Point out each Plasmodium parasite and each leukocyte.
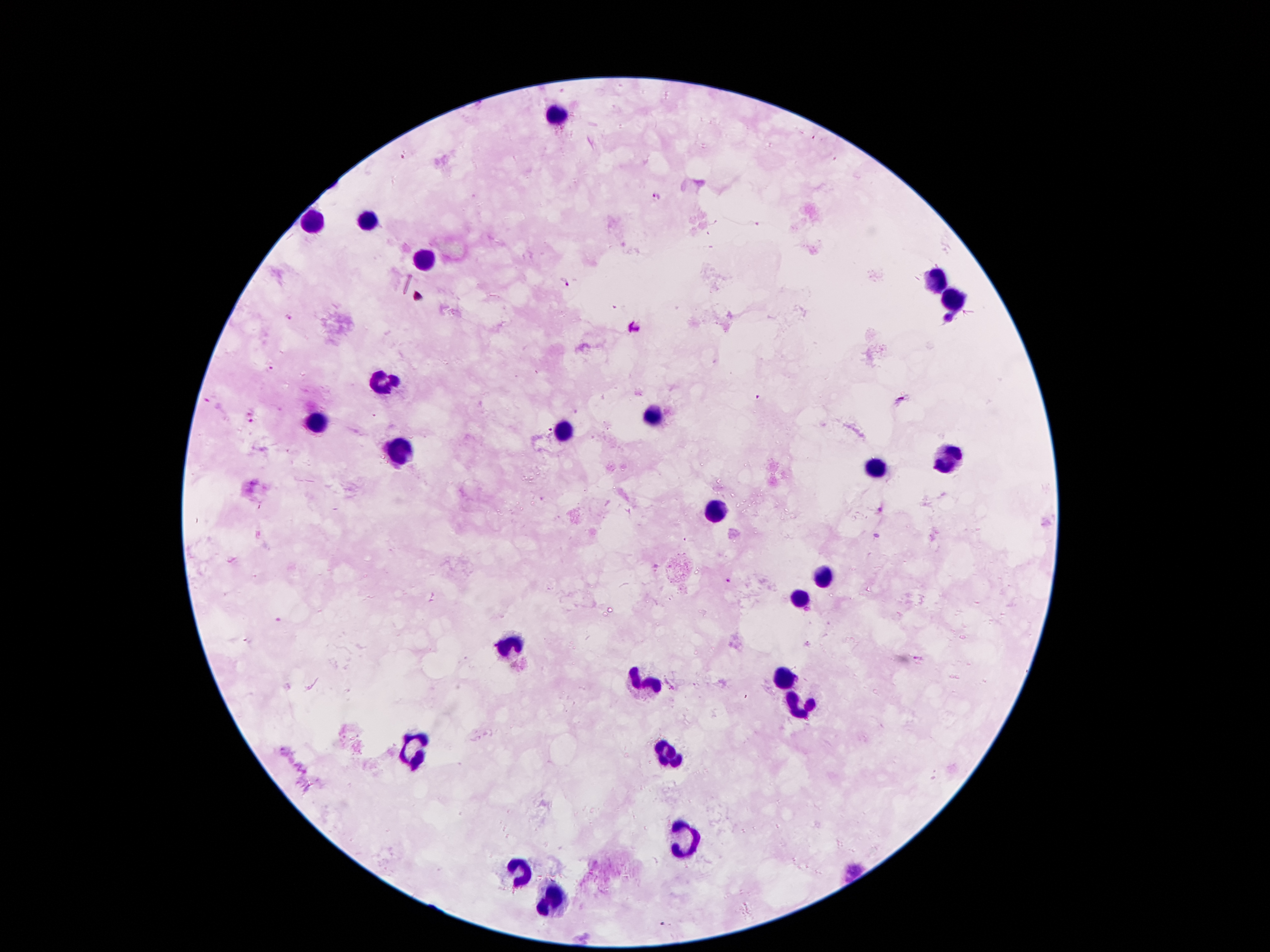

Approximate centers as {x, y} in pixels.
Plasmodium parasites: {656, 197}, {563, 283}, {288, 318}, {949, 320}, {632, 328}, {270, 368}, {757, 397}, {901, 400}, {251, 412}, {251, 421}, {881, 509}, {728, 580}.
Leukocytes: {560, 114}, {369, 220}, {313, 222}, {423, 262}, {938, 280}, {955, 299}, {383, 380}, {651, 416}, {315, 422}, {563, 429}, {397, 451}, {950, 461}, {878, 468}, {715, 509}, {822, 579}, {801, 600}, {514, 643}, {784, 676}, {645, 682}, {799, 706}, {411, 745}, {670, 752}, {684, 843}, {518, 872}, {551, 901}.

patient_malaria_status: infected with Plasmodium falciparum
image_size: 1270×952 pixels
capture: smartphone camera through the microscope eyepiece
stain: Giemsa
field_of_view: one from this slide
preparation: thick blood smear
magnification: 100x